Classify this cell by malaria status.
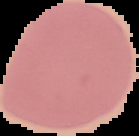

It is uninfected.

Summary:
  - Image type: segmented cell region on a black background
  - Preparation: thin blood smear
  - Image size: 139×136 pixels